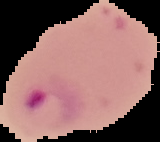

Malaria status: parasitized. Image is 160×142 pixels. From a thin blood film. Segmented cell region on a black background.